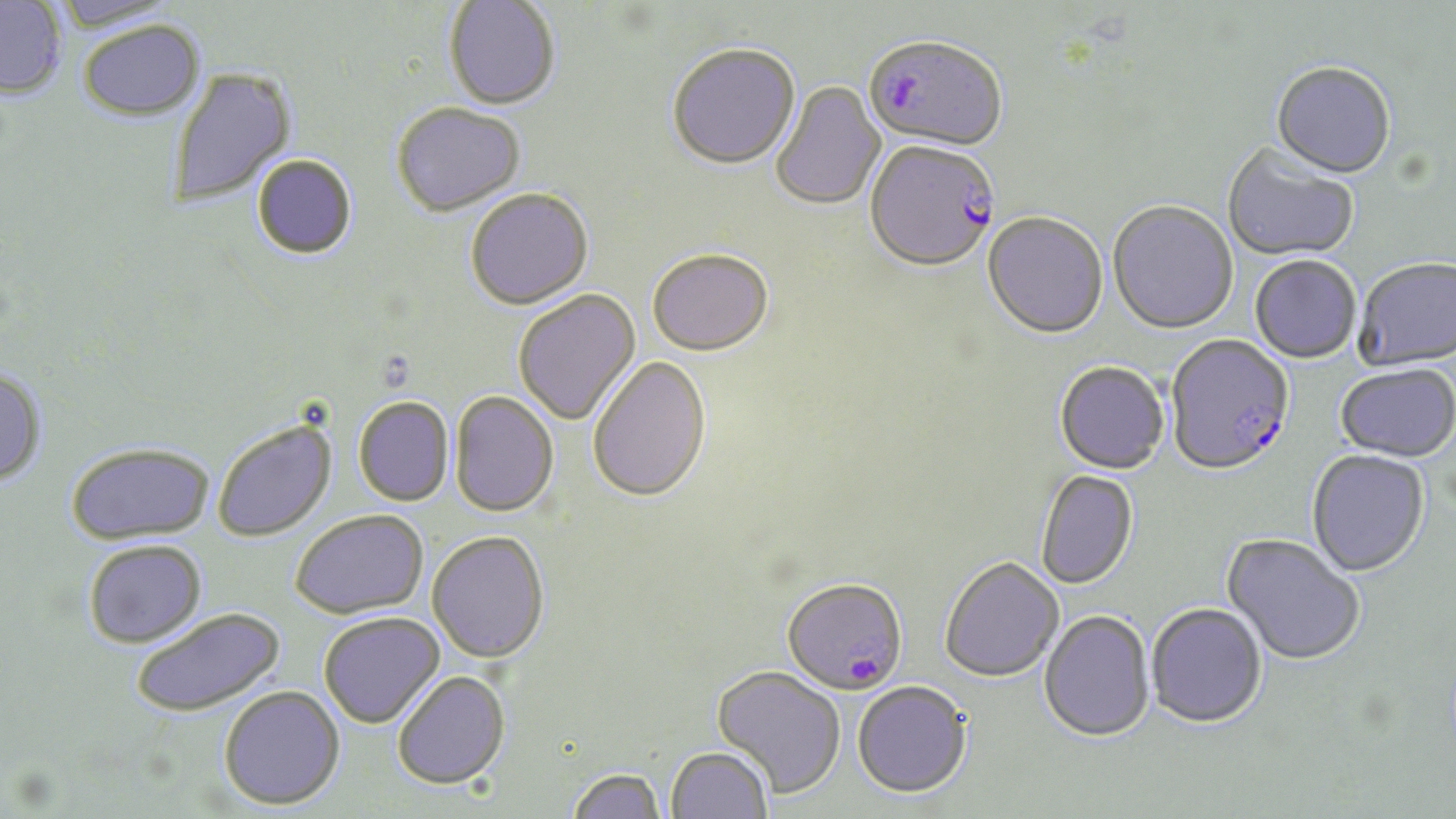

{
  "plasmodium_falciparum_infected_red_blood_cell_locations": "approximate bounding boxes as [x1, y1, x2, y2] in pixels: [864, 38, 1007, 155], [866, 144, 1001, 275], [1165, 336, 1296, 478], [782, 579, 908, 698]",
  "slide_level_diagnosis": "Plasmodium falciparum",
  "image_size": "1456×819 pixels",
  "modality": "optical microscopy",
  "preparation": "thin blood smear",
  "field_of_view": "one of a larger specimen",
  "magnification": "1000x",
  "stain": "May-Grünwald-Giemsa",
  "uninfected_red_blood_cell_locations": "approximate bounding boxes as [x1, y1, x2, y2] in pixels: [53, 0, 182, 33], [0, 1, 67, 99], [444, 1, 560, 113], [78, 22, 206, 123], [667, 46, 801, 173], [1270, 64, 1396, 182], [167, 66, 297, 210], [771, 81, 887, 212], [392, 104, 526, 219], [1222, 145, 1359, 263], [251, 155, 357, 261], [465, 190, 593, 312], [1107, 202, 1238, 337], [982, 214, 1108, 342], [647, 252, 773, 358], [1250, 258, 1361, 365], [1354, 260, 1456, 373], [513, 290, 642, 427], [588, 355, 712, 504], [1054, 363, 1170, 476], [1334, 365, 1456, 466], [0, 368, 48, 486], [450, 391, 559, 518], [354, 397, 455, 506], [212, 418, 337, 542], [66, 442, 214, 544], [1306, 451, 1430, 579], [1035, 471, 1139, 592], [290, 510, 428, 619], [427, 530, 550, 663], [1220, 535, 1364, 668], [83, 540, 206, 648], [940, 559, 1064, 684], [1146, 605, 1267, 731], [130, 607, 284, 718], [318, 612, 444, 728], [1038, 612, 1156, 745], [711, 666, 846, 800], [391, 670, 511, 789], [851, 683, 973, 801], [218, 685, 345, 809], [665, 746, 773, 819], [566, 767, 665, 819]"
}